Report the malaria status of this cell.
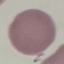

Uninfected.

capture = smartphone through the microscope eyepiece
image type = automatically extracted cell patch, resized to 64 × 64 pixels
stain = Giemsa
preparation = thin blood film